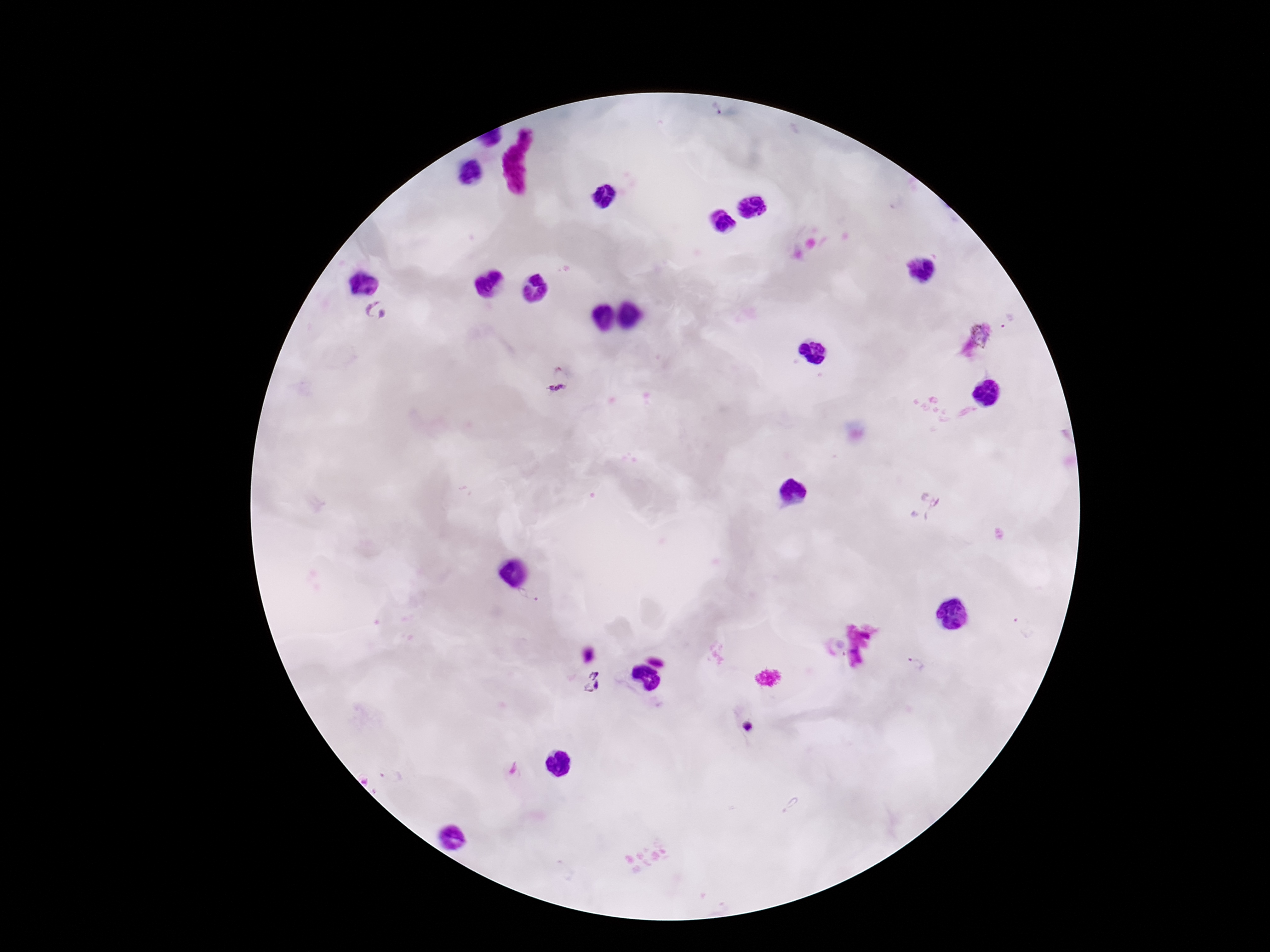

Approximate centers as {x, y} in pixels. Plasmodium parasite locations: {377, 311}, {983, 332}, {558, 388}, {925, 505}, {528, 597}, {1024, 627}, {915, 663}, {591, 682}. Patient malaria status: positive. Thick peripheral-blood smear. Single field of view. 100x magnification. Image is 1270×952 pixels. Giemsa stain. Photographed through the microscope eyepiece with a smartphone camera.